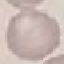

Malaria status: uninfected. Acquired by smartphone through the microscope eyepiece. Thin blood smear. Automatically extracted cell patch, resized to 64 × 64 pixels. Giemsa stain.